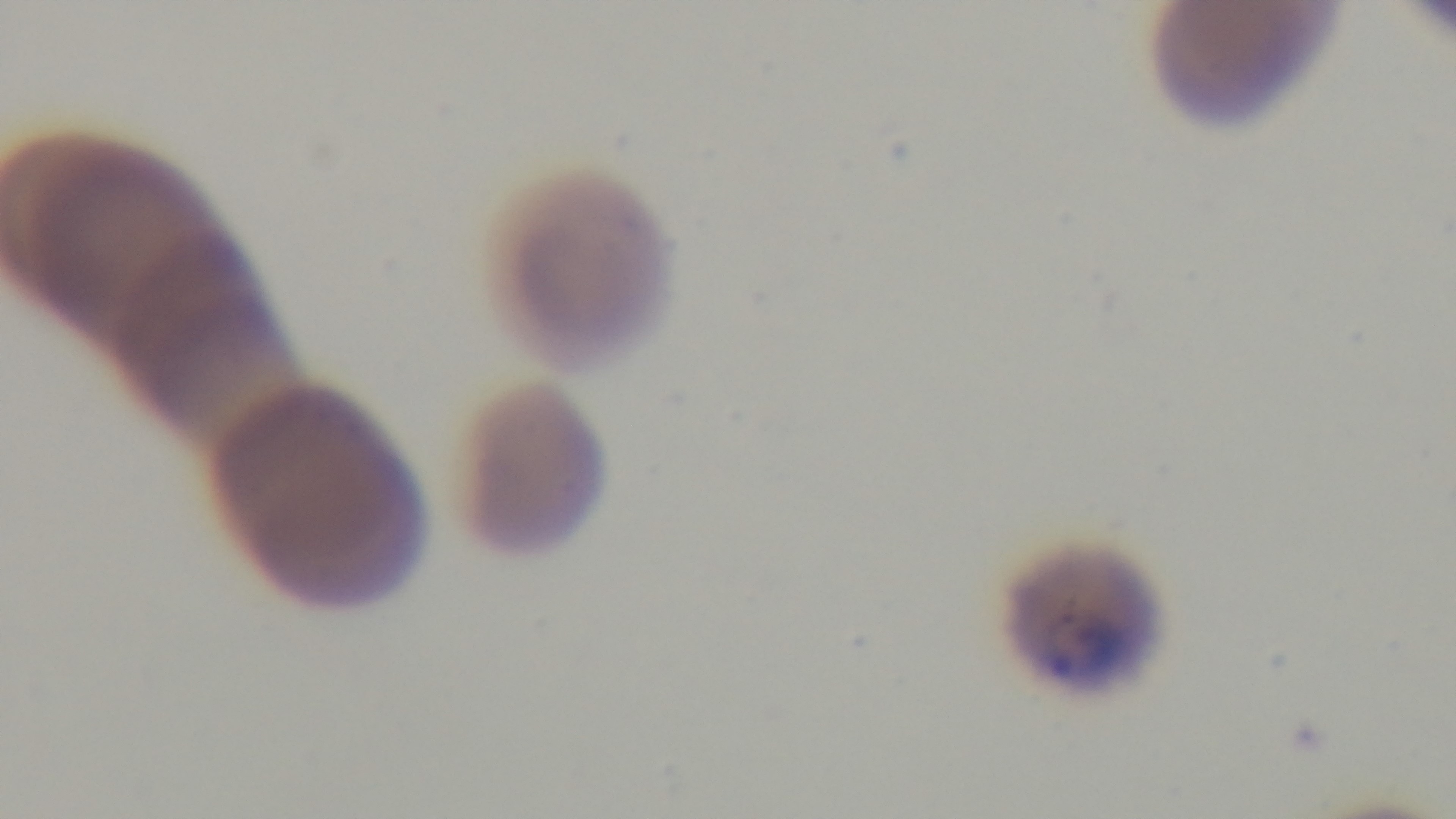

Summary:
  - Modality: light microscopy
  - Capture: mounted 4K digital camera
  - Malaria status: positive
  - Field of view: single
  - Preparation: thin
  - Objective: 100x oil immersion
  - Stain: Giemsa